Point out each malaria parasite.
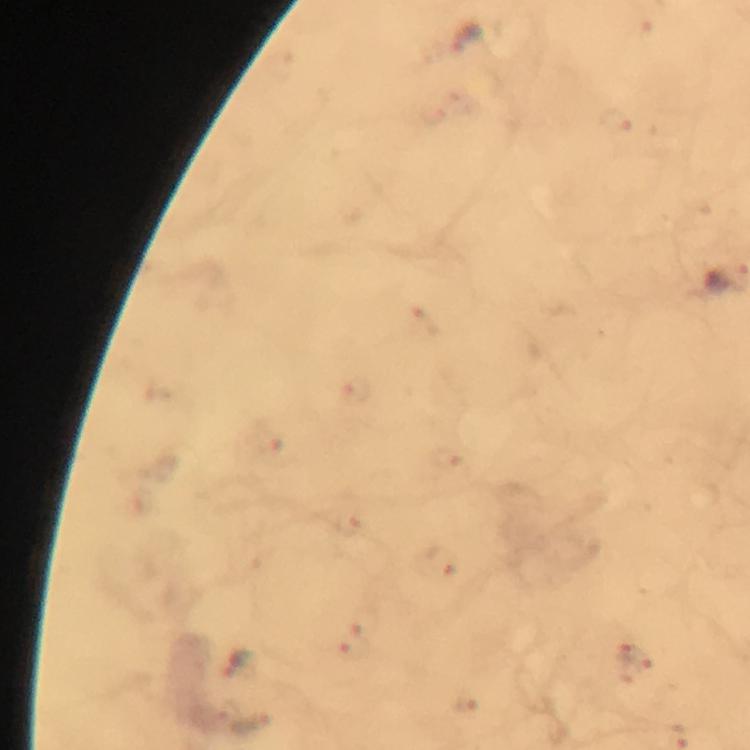
Approximate object centers, in pixels from the top-left corner.
Malaria parasites: (x=426, y=322), (x=357, y=390), (x=267, y=442), (x=448, y=458), (x=348, y=525), (x=443, y=563), (x=363, y=625), (x=347, y=651), (x=636, y=658), (x=237, y=664), (x=467, y=704).

{
  "magnification": "100x",
  "capture": "smartphone photograph through a microscope",
  "stain": "Giemsa",
  "image_size": "750×750 pixels",
  "immersion_oil": "used",
  "cropped_from": "one field of view",
  "preparation": "thick blood film",
  "context": "from a diagnostic examination for malaria"
}